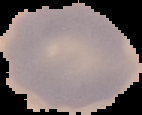

Summary:
  - Preparation: thin blood film
  - Image type: segmented cell region on a black background
  - Malaria status: uninfected
  - Image size: 142×115 pixels